State the preparation type.
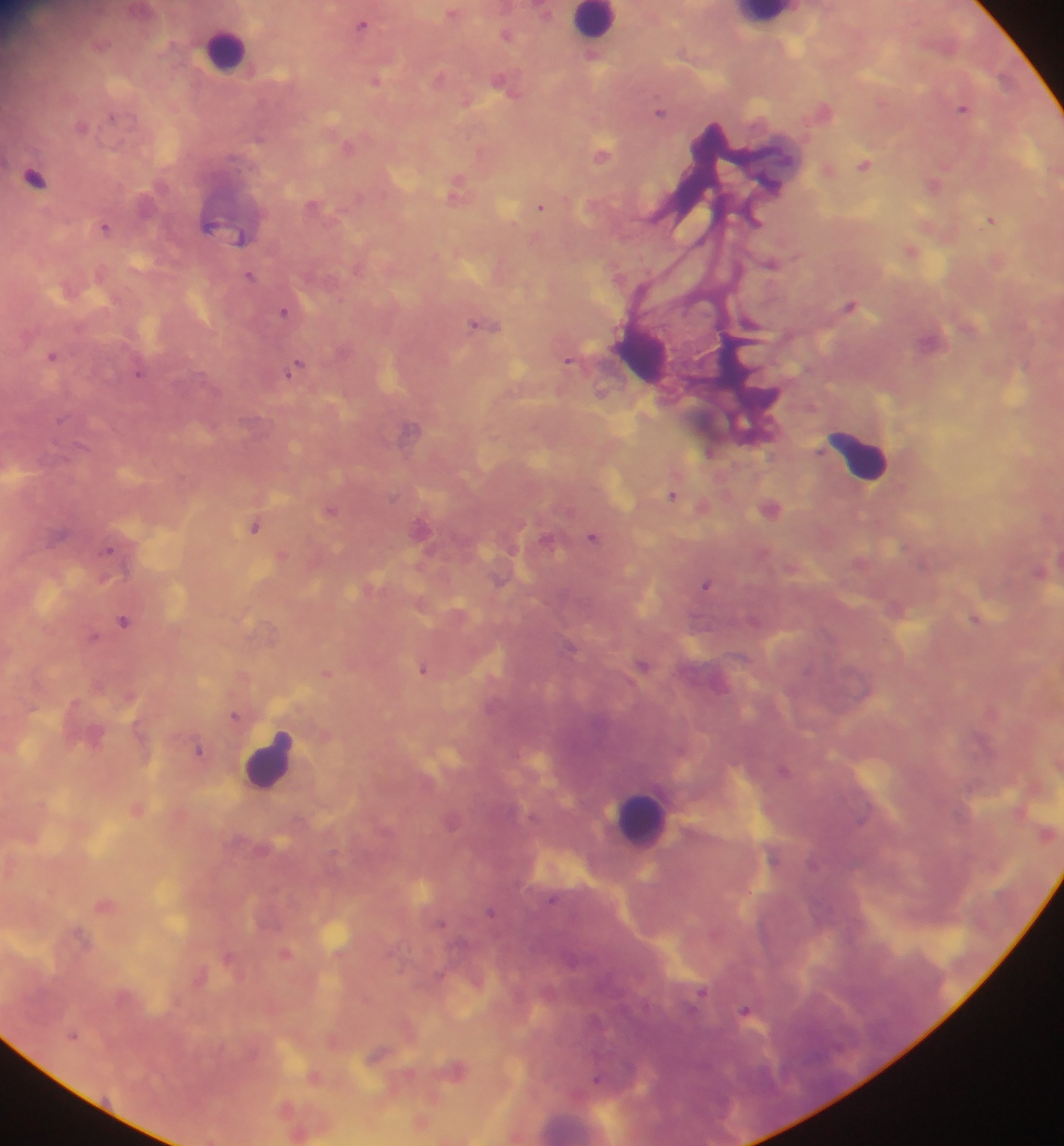
Thick blood smear.

Approximate centers as [x, y] in pixels.
Summary:
  - Leukocyte locations: [767, 16], [594, 22], [224, 50], [642, 353], [858, 454], [269, 760], [641, 817], [571, 1124]
  - Plasmodium parasite locations: [545, 10], [453, 13], [363, 24], [507, 33], [440, 77], [376, 80], [507, 84], [963, 108], [823, 110], [660, 111], [349, 146], [603, 153], [865, 164], [830, 169], [35, 177], [934, 184], [458, 187], [314, 204], [541, 207], [755, 220], [992, 220], [210, 224], [106, 226], [225, 228], [242, 238], [911, 251], [772, 263], [250, 276], [851, 304], [286, 312], [483, 324], [932, 342], [53, 356], [570, 360], [297, 367], [140, 373], [412, 428], [709, 452], [673, 494], [702, 506], [770, 508], [332, 510], [256, 525], [421, 529], [593, 537], [548, 539], [283, 556], [1040, 572], [707, 584], [895, 607], [977, 619], [124, 620], [94, 637], [571, 646], [644, 666], [425, 669], [327, 672], [244, 677], [236, 716], [200, 750], [784, 770], [137, 808], [452, 822], [553, 900], [106, 903], [491, 911], [441, 924], [286, 953], [229, 956], [201, 976], [701, 992], [747, 1013], [73, 1033], [334, 1041], [378, 1055], [457, 1069], [315, 1076], [598, 1079], [421, 1122], [300, 1133]
  - Country: Ghana
  - Field of view: single
  - Capture: mobile-phone photograph through a microscope
  - Image size: 1064×1146 pixels